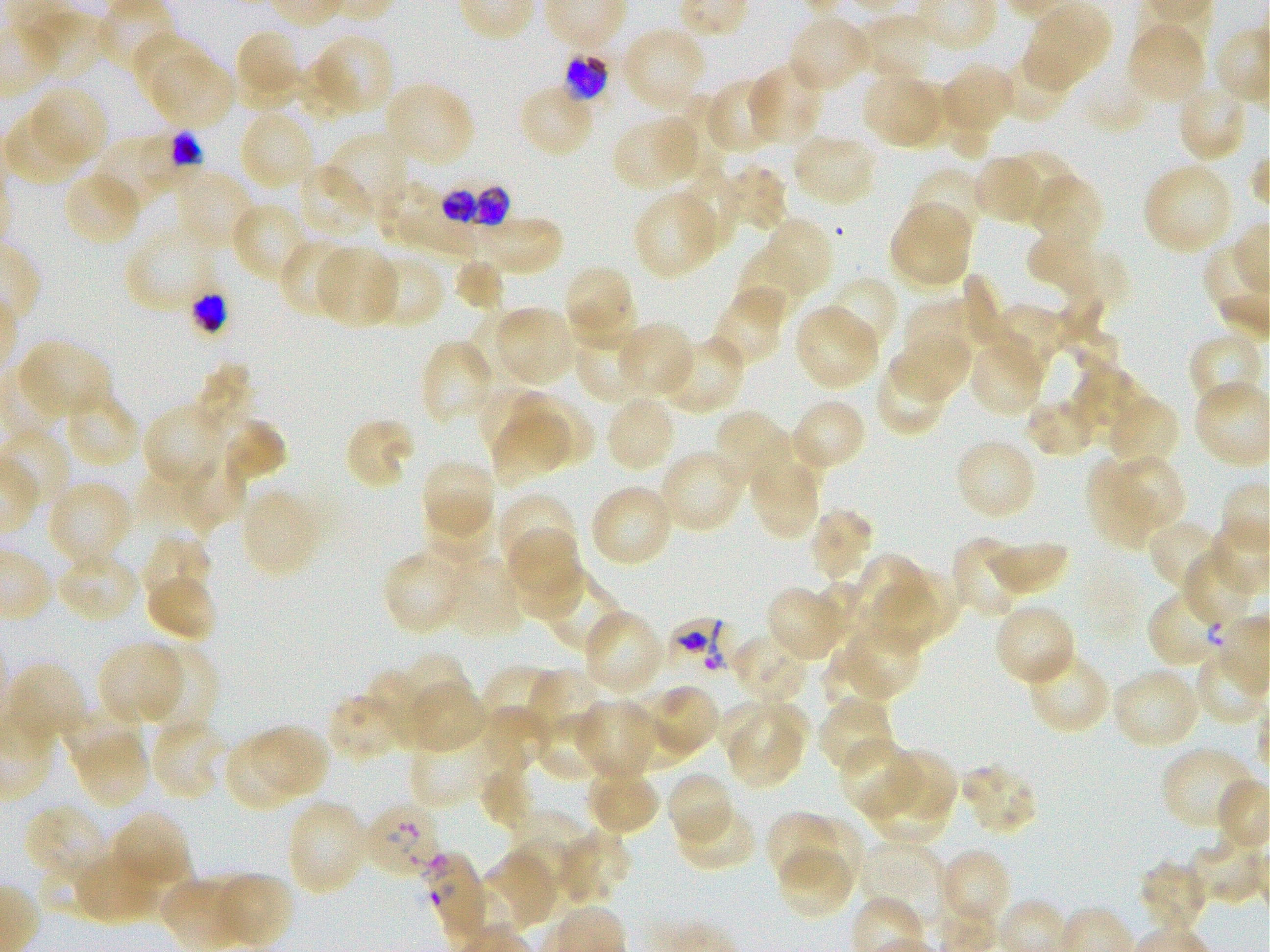 Approximate bounding boxes as (x1, y1, x2, y2) in pixels. Not every red blood cell is marked. A life-cycle stage — or a range of stages, where the recorded stages span more than one — follows each staged infected red blood cell. Locations of uninfected red blood cells: (1025, 3, 1110, 87), (861, 13, 929, 77), (787, 14, 872, 93), (32, 15, 105, 80), (1127, 23, 1206, 103), (622, 26, 706, 111), (241, 28, 303, 92), (132, 31, 209, 106), (313, 34, 395, 115), (1003, 49, 1074, 124), (152, 53, 233, 129), (237, 55, 299, 111), (749, 62, 824, 145), (294, 63, 357, 121), (941, 64, 1014, 136), (861, 72, 937, 145), (707, 78, 777, 155), (1083, 78, 1148, 134), (890, 80, 959, 150), (383, 81, 476, 167), (1175, 82, 1248, 163), (517, 85, 596, 158), (29, 86, 108, 167), (680, 93, 733, 170), (944, 103, 994, 161), (239, 108, 316, 190), (4, 112, 87, 186), (614, 121, 699, 187), (327, 131, 410, 215), (791, 132, 878, 207), (97, 141, 167, 211), (1006, 149, 1074, 222), (972, 154, 1038, 225), (297, 162, 374, 241), (1142, 162, 1233, 255), (725, 165, 788, 234), (908, 166, 985, 245), (675, 167, 740, 250), (174, 171, 257, 252), (63, 172, 143, 247), (1029, 175, 1102, 243), (380, 183, 442, 241), (632, 190, 719, 279), (230, 201, 308, 282), (891, 207, 971, 283), (1025, 208, 1097, 293), (472, 217, 562, 274), (768, 220, 834, 293), (124, 223, 214, 312), (278, 238, 355, 320), (1041, 238, 1128, 317), (736, 244, 807, 324), (314, 245, 399, 328), (366, 255, 446, 330), (451, 258, 503, 311), (568, 269, 633, 331), (961, 273, 1009, 351), (825, 276, 899, 356), (1055, 285, 1118, 370), (711, 288, 787, 367), (572, 298, 637, 349), (903, 298, 978, 375), (990, 304, 1063, 382), (494, 306, 574, 385), (794, 306, 881, 390), (471, 308, 537, 381), (616, 322, 695, 398), (574, 329, 649, 405), (890, 333, 971, 400), (1189, 333, 1265, 413), (659, 334, 746, 416), (970, 338, 1045, 417), (419, 339, 497, 425), (19, 340, 112, 421), (875, 356, 949, 437), (196, 364, 262, 435), (1073, 364, 1135, 427), (1082, 379, 1149, 443), (475, 383, 550, 459), (63, 390, 142, 468), (513, 391, 594, 468), (604, 395, 677, 473), (1026, 396, 1096, 457), (1110, 399, 1177, 464), (791, 402, 863, 467), (143, 404, 229, 488), (713, 410, 789, 490), (343, 415, 415, 491), (491, 415, 564, 486), (223, 420, 287, 483), (748, 430, 825, 494), (953, 438, 1038, 521), (657, 447, 746, 533), (177, 451, 246, 529), (421, 457, 496, 537), (1113, 458, 1185, 525), (134, 462, 203, 533), (1085, 462, 1154, 548), (753, 466, 821, 538), (47, 480, 133, 569), (589, 483, 674, 568), (242, 490, 321, 578), (498, 493, 578, 573), (421, 501, 495, 566), (807, 507, 875, 580), (1147, 518, 1221, 589), (508, 522, 580, 594), (143, 535, 213, 605), (950, 536, 1024, 618), (988, 539, 1069, 595), (55, 548, 139, 623), (382, 549, 468, 635), (1182, 549, 1257, 623), (511, 550, 583, 619), (853, 553, 928, 630), (445, 557, 526, 639), (904, 570, 957, 636), (542, 572, 624, 656), (145, 574, 218, 642), (875, 578, 939, 657), (809, 580, 866, 648), (766, 586, 844, 661), (993, 602, 1076, 686), (582, 610, 666, 694), (840, 622, 921, 700), (729, 632, 808, 705), (97, 641, 183, 723), (142, 644, 219, 735), (821, 646, 884, 715), (1026, 648, 1111, 735), (400, 653, 468, 719), (8, 662, 87, 744), (480, 664, 556, 732), (525, 667, 606, 746), (1112, 667, 1200, 750), (364, 670, 430, 748), (409, 685, 486, 755), (651, 685, 718, 753), (623, 690, 691, 769), (324, 691, 403, 763), (817, 698, 895, 777), (575, 699, 657, 781), (62, 702, 142, 771), (717, 702, 810, 757), (482, 703, 551, 772), (533, 711, 607, 783), (729, 716, 804, 787), (149, 719, 227, 801), (249, 723, 329, 799), (223, 733, 303, 811), (80, 734, 150, 809), (409, 737, 490, 809), (838, 738, 919, 820), (1160, 745, 1258, 831), (884, 746, 957, 819), (961, 762, 1038, 836), (480, 766, 535, 831), (585, 766, 660, 835), (667, 771, 734, 849), (865, 777, 950, 847), (291, 803, 364, 890), (676, 803, 758, 872), (24, 804, 108, 886), (510, 809, 586, 875), (765, 811, 836, 885), (116, 813, 189, 881), (796, 816, 863, 893), (556, 830, 633, 905), (513, 835, 573, 890), (1188, 839, 1266, 905), (860, 841, 946, 928), (778, 845, 855, 919), (72, 848, 160, 925), (125, 849, 195, 921), (939, 849, 1011, 929), (484, 850, 559, 928), (1138, 859, 1209, 933), (220, 874, 294, 947). Locations of red blood cells of indeterminate infection status: (428, 853, 485, 934). Locations of infected red blood cells: (562, 53, 611, 103) late trophozoite to early schizont; (137, 129, 203, 190); (444, 179, 507, 249); (189, 285, 228, 333) early trophozoite to late schizont; (1149, 591, 1224, 663) late ring; (670, 606, 734, 678); (367, 801, 443, 875). Single field of view. Thin blood smear. P. falciparum strain 3D7 maintained in static in-vitro culture. Oil immersion, 100x objective (numerical aperture 1.25). Image is 1270×952 pixels. Blood group of the donor: O+. Giemsa stain.